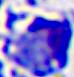
Photomicrograph. A leukocyte is shown. Captured at 400x magnification.